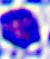 400x magnification. Micrograph. A white blood cell is shown.